Assess the morphology of the red blood cells.
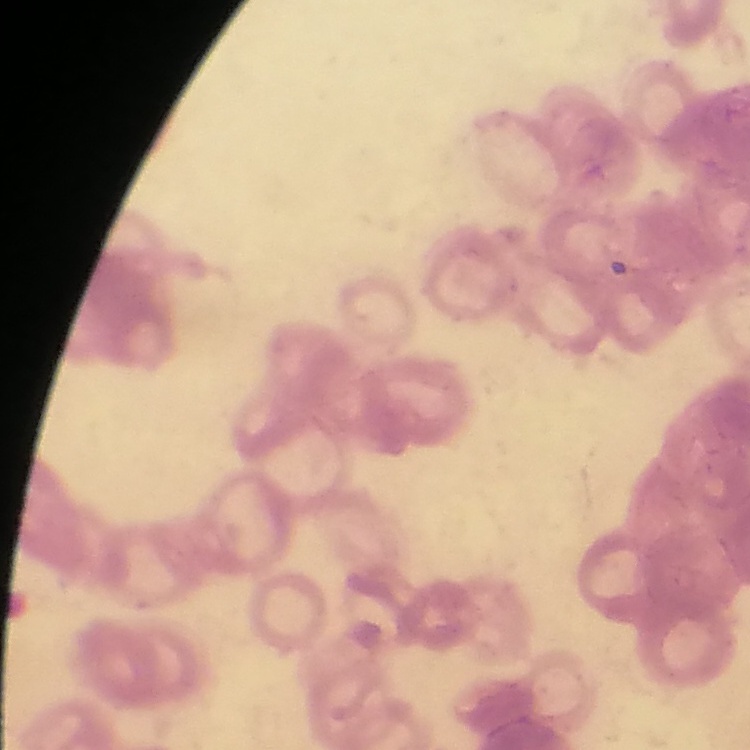
Rouleaux formation.

Stained with either Field's or Giemsa. Thin peripheral smear. Square crop of a larger photomicrograph.